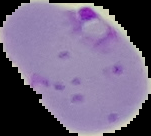

image_type: cell region segmented out of the field of view; surrounding area masked to black
image_size: 151×136 pixels
malaria_status: parasitized
preparation: thin blood film